State which cell type is depicted.
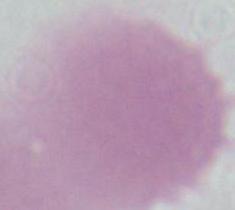
An erythrocyte.

Captured at 1000x magnification. Photomicrograph.